Describe the morphology of the erythrocytes.
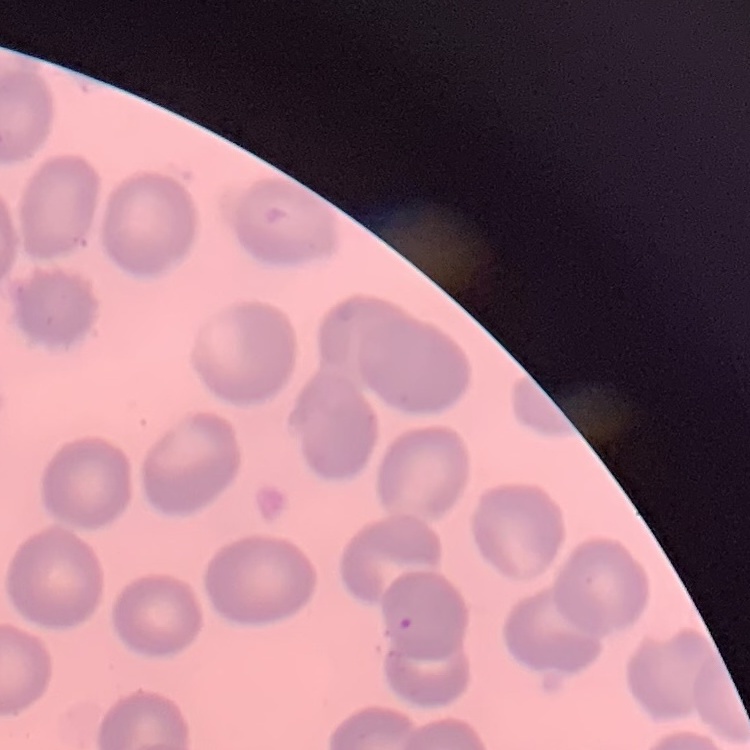

No rouleaux formation.

Summary:
  - Preparation: thin blood smear
  - Stain: Field's or Giemsa
  - Image type: square crop of a larger photomicrograph